Report the malaria status.
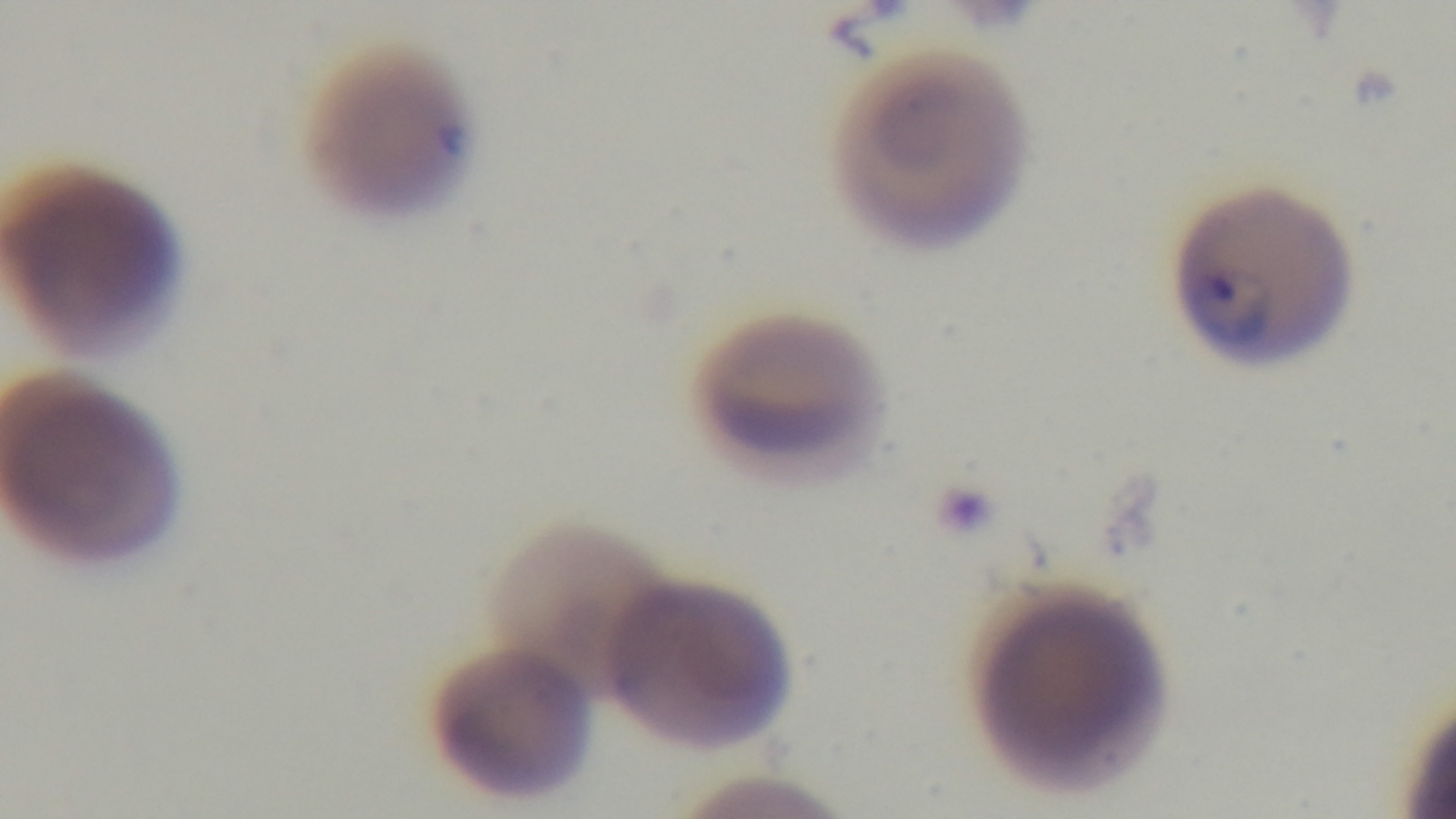

It is infected.

Single field of view. Captured with a mounted 4K digital camera. Giemsa-stained. Oil-immersion objective, 100x. Photomicrograph. Preparation: thin.